Outline each blood parasite and name the species.
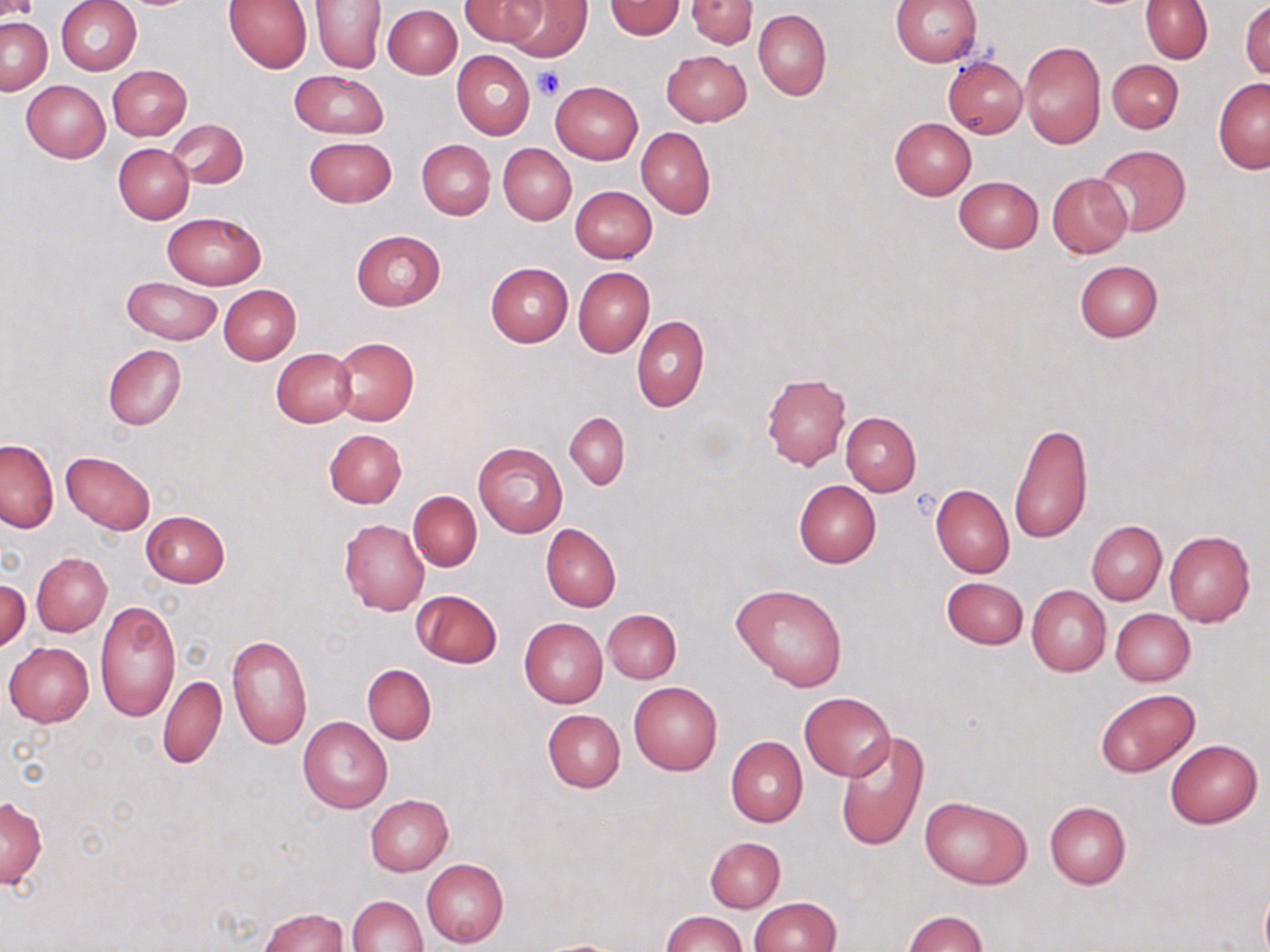

No blood parasites observed.

Summary:
  - Coordinate format: approximate bounding boxes as (x1, y1, x2, y2) in pixels
  - Platelet locations: (534, 67, 565, 99)
  - Uninfected red blood cell locations: (0, 0, 37, 22), (56, 0, 142, 75), (460, 0, 545, 48), (502, 0, 591, 61), (605, 0, 684, 39), (686, 0, 756, 48), (892, 0, 982, 66), (221, 1, 312, 73), (311, 1, 386, 73), (1140, 1, 1213, 63), (1240, 1, 1269, 81), (383, 4, 462, 79), (753, 9, 830, 100), (0, 17, 51, 94), (1019, 40, 1106, 148), (661, 50, 752, 126), (452, 51, 535, 139), (943, 56, 1027, 138), (1108, 59, 1184, 134), (107, 64, 192, 139), (289, 70, 388, 139), (1212, 78, 1269, 174), (22, 80, 110, 162), (551, 81, 644, 164), (889, 117, 976, 199), (168, 120, 248, 188), (636, 127, 716, 219), (305, 136, 395, 207), (417, 139, 495, 219), (113, 144, 194, 224), (497, 144, 576, 225), (1092, 144, 1191, 235), (1047, 172, 1132, 258), (953, 176, 1044, 253), (570, 186, 657, 264), (162, 211, 266, 289), (352, 229, 445, 310), (1074, 260, 1163, 342), (485, 262, 573, 347), (573, 267, 654, 357), (122, 276, 221, 344), (218, 283, 301, 365), (632, 315, 709, 411), (331, 336, 419, 426), (103, 344, 187, 430), (272, 348, 357, 427), (761, 373, 850, 470), (564, 411, 629, 489), (840, 411, 921, 496), (1009, 420, 1092, 545), (324, 430, 407, 508), (0, 439, 58, 532), (473, 442, 567, 537), (62, 451, 155, 534), (794, 480, 881, 568), (931, 485, 1014, 577), (409, 491, 481, 572), (141, 510, 230, 586), (339, 519, 430, 615), (1086, 521, 1166, 605), (541, 524, 621, 611), (1164, 530, 1255, 627), (32, 552, 112, 636), (942, 576, 1028, 649), (1, 578, 30, 651), (730, 583, 848, 692), (1026, 585, 1111, 676), (412, 589, 502, 668), (96, 601, 180, 723), (1110, 608, 1195, 686), (602, 609, 681, 683), (519, 617, 608, 708), (225, 633, 312, 751), (4, 642, 94, 726), (362, 664, 437, 743), (158, 675, 226, 769), (629, 682, 723, 775), (1094, 687, 1200, 777), (799, 691, 896, 781), (543, 709, 625, 793), (298, 715, 393, 813), (836, 733, 927, 851), (726, 737, 807, 827), (1164, 739, 1263, 828), (365, 794, 453, 876), (918, 795, 1032, 889), (0, 797, 48, 888), (1044, 801, 1130, 889), (705, 836, 785, 913), (422, 857, 509, 947), (1259, 883, 1270, 952), (347, 894, 427, 951), (751, 897, 840, 952), (259, 907, 349, 952), (661, 911, 745, 952), (905, 911, 989, 952), (535, 938, 630, 951)
  - Slide-level diagnosis: no evidence of blood parasites
  - Field of view: single
  - Image size: 1270×952 pixels
  - Stain: May-Grünwald-Giemsa
  - Preparation: thin blood smear
  - Magnification: 1000x
  - Modality: light microscopy